Point out each Plasmodium parasite and each leukocyte.
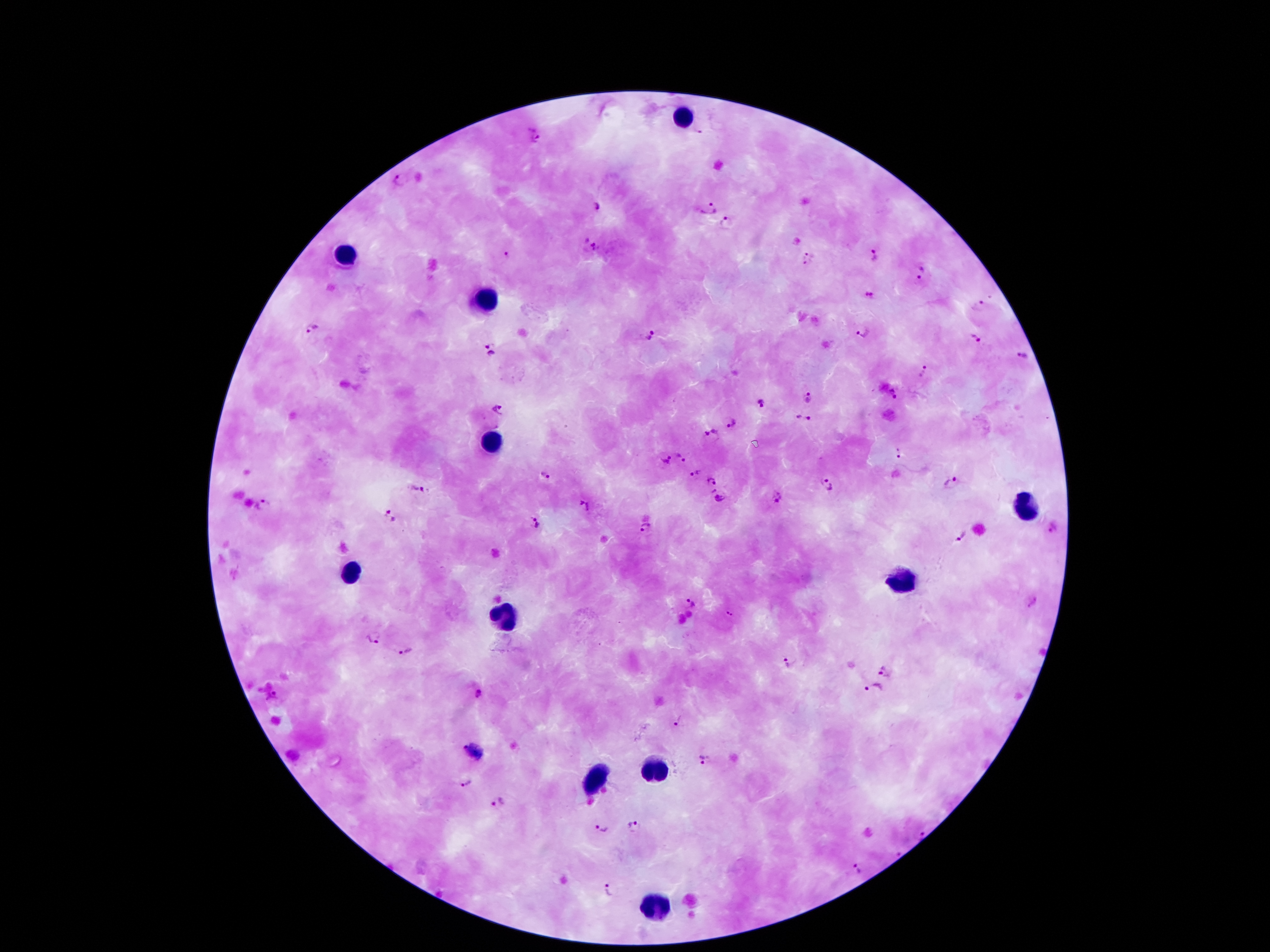

Approximate object centers, in pixels from the top-left corner.
Plasmodium parasites: (x=535, y=135), (x=401, y=180), (x=595, y=205), (x=710, y=209), (x=727, y=223), (x=592, y=247), (x=507, y=255), (x=875, y=255), (x=809, y=258), (x=920, y=273), (x=871, y=296), (x=979, y=305), (x=312, y=330), (x=865, y=333), (x=649, y=338), (x=974, y=339), (x=490, y=349), (x=1021, y=356), (x=923, y=371), (x=893, y=393), (x=809, y=395), (x=761, y=405), (x=498, y=411), (x=803, y=417), (x=730, y=423), (x=711, y=432), (x=682, y=453), (x=898, y=454), (x=666, y=459), (x=695, y=473), (x=545, y=476), (x=709, y=481), (x=829, y=484), (x=953, y=484), (x=419, y=488), (x=719, y=498), (x=777, y=499), (x=265, y=504), (x=586, y=508), (x=389, y=517), (x=538, y=523), (x=646, y=529), (x=1054, y=529), (x=962, y=537), (x=690, y=602), (x=729, y=613), (x=374, y=639), (x=406, y=651), (x=787, y=662), (x=884, y=669), (x=873, y=686), (x=476, y=693), (x=271, y=696), (x=677, y=721), (x=460, y=747), (x=703, y=759), (x=468, y=784), (x=497, y=803), (x=602, y=824), (x=632, y=825), (x=922, y=833), (x=856, y=868), (x=610, y=890).
Leukocytes: (x=680, y=119), (x=347, y=250), (x=485, y=302), (x=488, y=443), (x=1026, y=510), (x=349, y=571), (x=898, y=579), (x=502, y=618), (x=653, y=774), (x=591, y=776), (x=653, y=907).

capture: smartphone through the microscope eyepiece
magnification: 100x
stain: Giemsa
preparation: thick blood film
image_size: 1270×952 pixels
patient_malaria_status: infected with Plasmodium falciparum
field_of_view: one from this slide